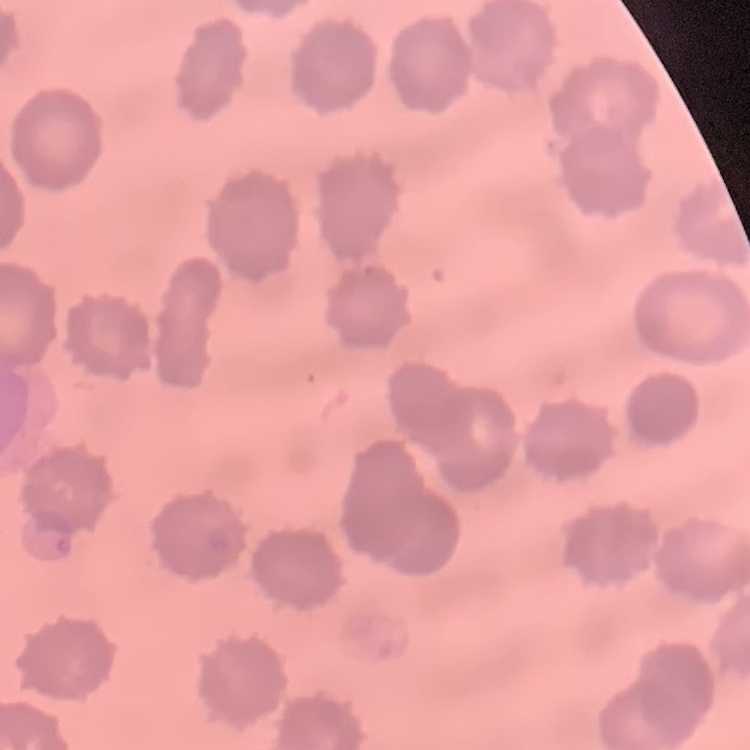

erythrocyte_morphology: no rouleaux formation
image_type: one tile cut from a larger photomicrograph
stain: Field's or Giemsa
preparation: thin peripheral smear